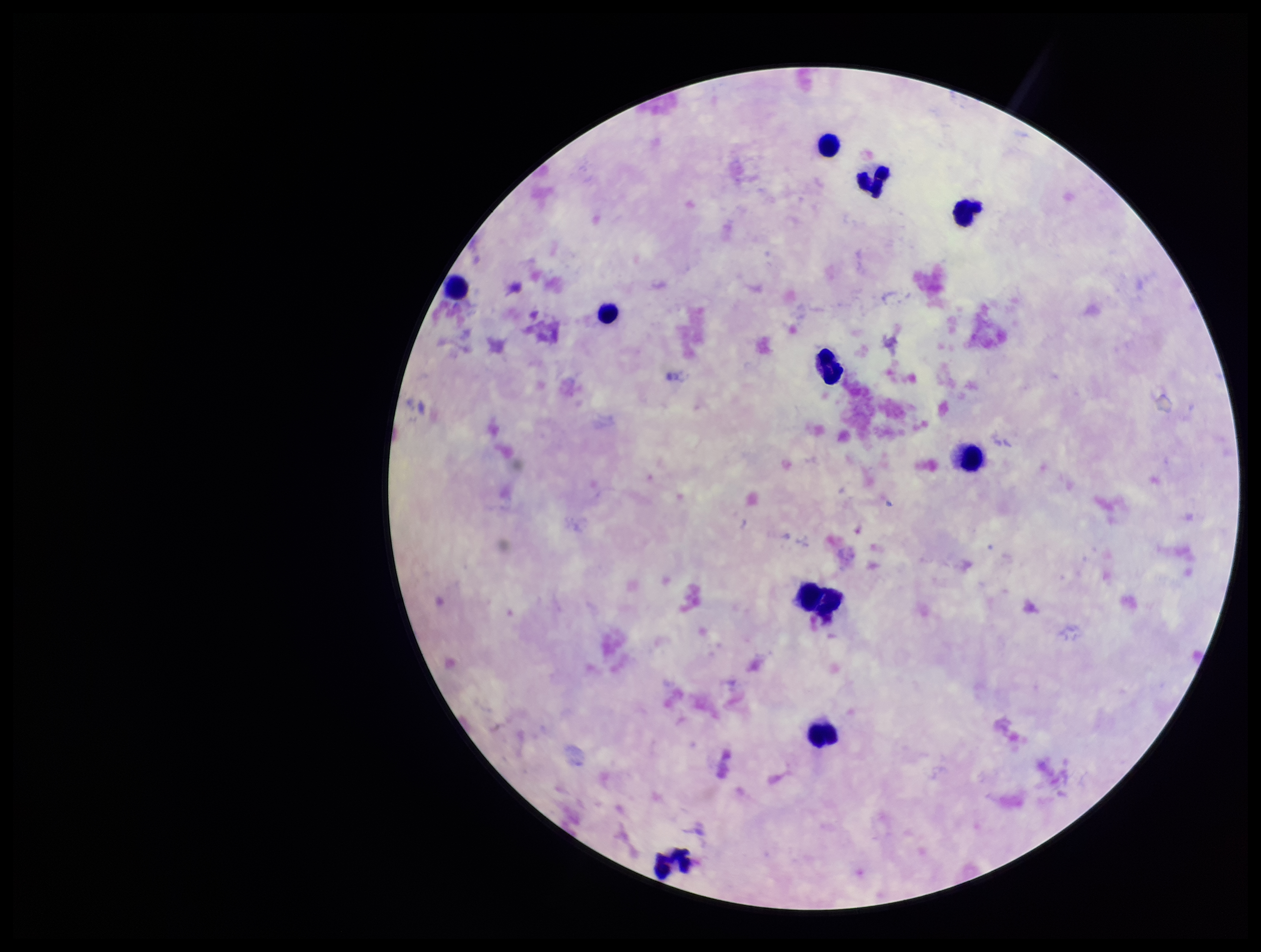
{
  "field_of_view": "single",
  "parasite_count": 0,
  "stain": "Giemsa",
  "leukocyte_count": 10,
  "capture": "smartphone photograph through the microscope eyepiece",
  "image_size": "1261×952 pixels",
  "patient_malaria_status": "negative",
  "preparation": "thick blood smear",
  "plasmodium_parasites": "none detected"
}